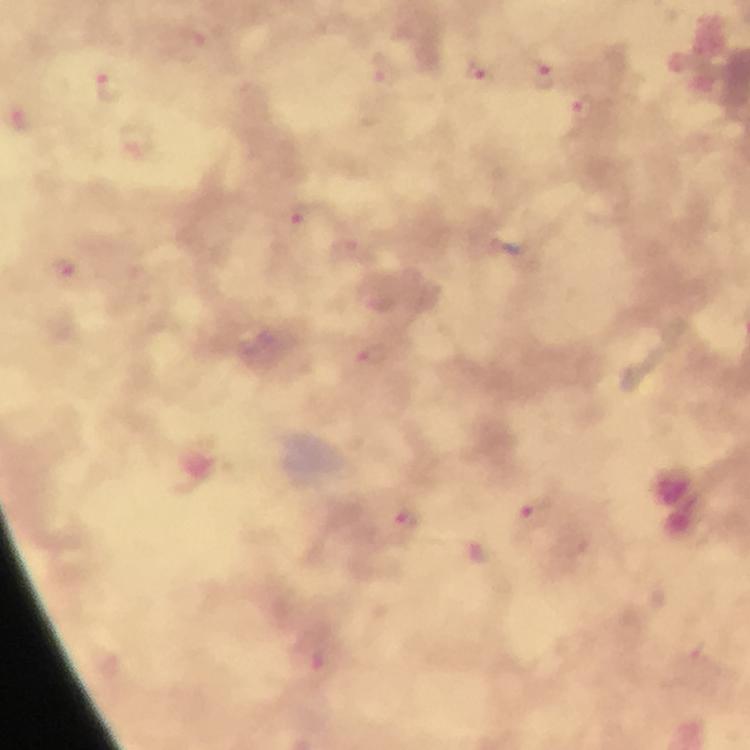

context: from a diagnostic examination for malaria
preparation: thick blood smear
cropped_from: one field of view
malaria_parasite_locations: 'approximate centers as (x, y) in pixels: (192, 43), (383, 71), (479, 72), (539, 76), (109, 88), (585, 109), (22, 120), (136, 138), (298, 215), (61, 269), (369, 357), (531, 516), (404, 524), (322, 669)'
capture: smartphone camera through the microscope
image_size: 750×750 pixels
stain: Giemsa
magnification: 100x
immersion_oil: used